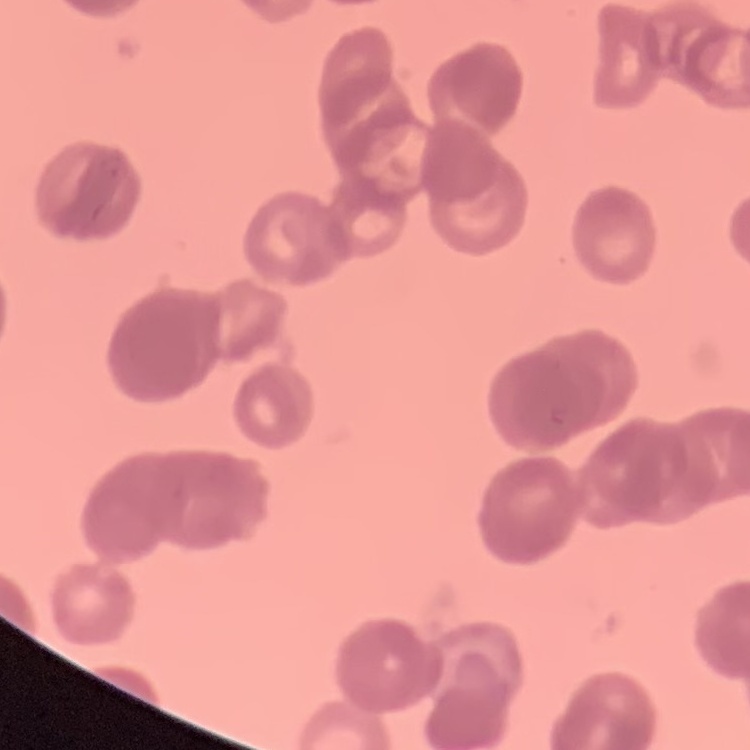

Summary:
  - Erythrocyte morphology: rouleaux formation
  - Image type: one tile cut from a larger photomicrograph
  - Stain: Field's or Giemsa
  - Preparation: thin blood smear